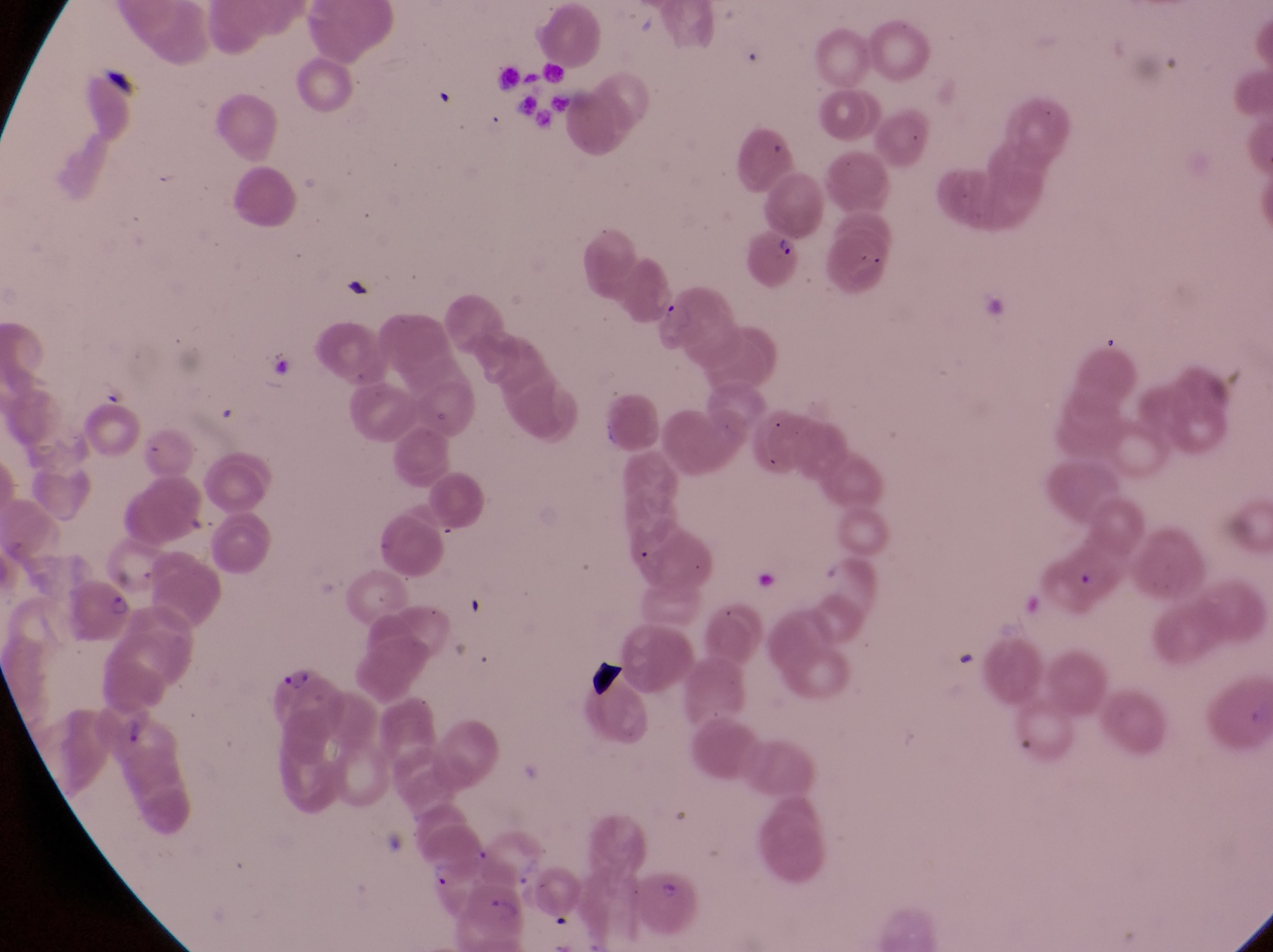 Approximate bounding boxes as [left, top, right, bottom] in pixels. Parasitised red blood cell locations: [756, 227, 809, 289], [654, 287, 741, 375], [60, 575, 142, 645], [267, 667, 344, 745], [102, 700, 160, 756], [470, 885, 527, 942]. Artifact (platelet-like body, stain precipitate, or debris) locations: [102, 57, 144, 104], [339, 274, 376, 304], [584, 659, 641, 706]. Image is 1273×952 pixels. Photographed through the eyepiece of an Olympus CX-23 microscope with a smartphone camera. Collected in Uganda. One field of view. Thin blood smear. Magnification of 1000x.